Locate every Plasmodium falciparum-infected red blood cell.
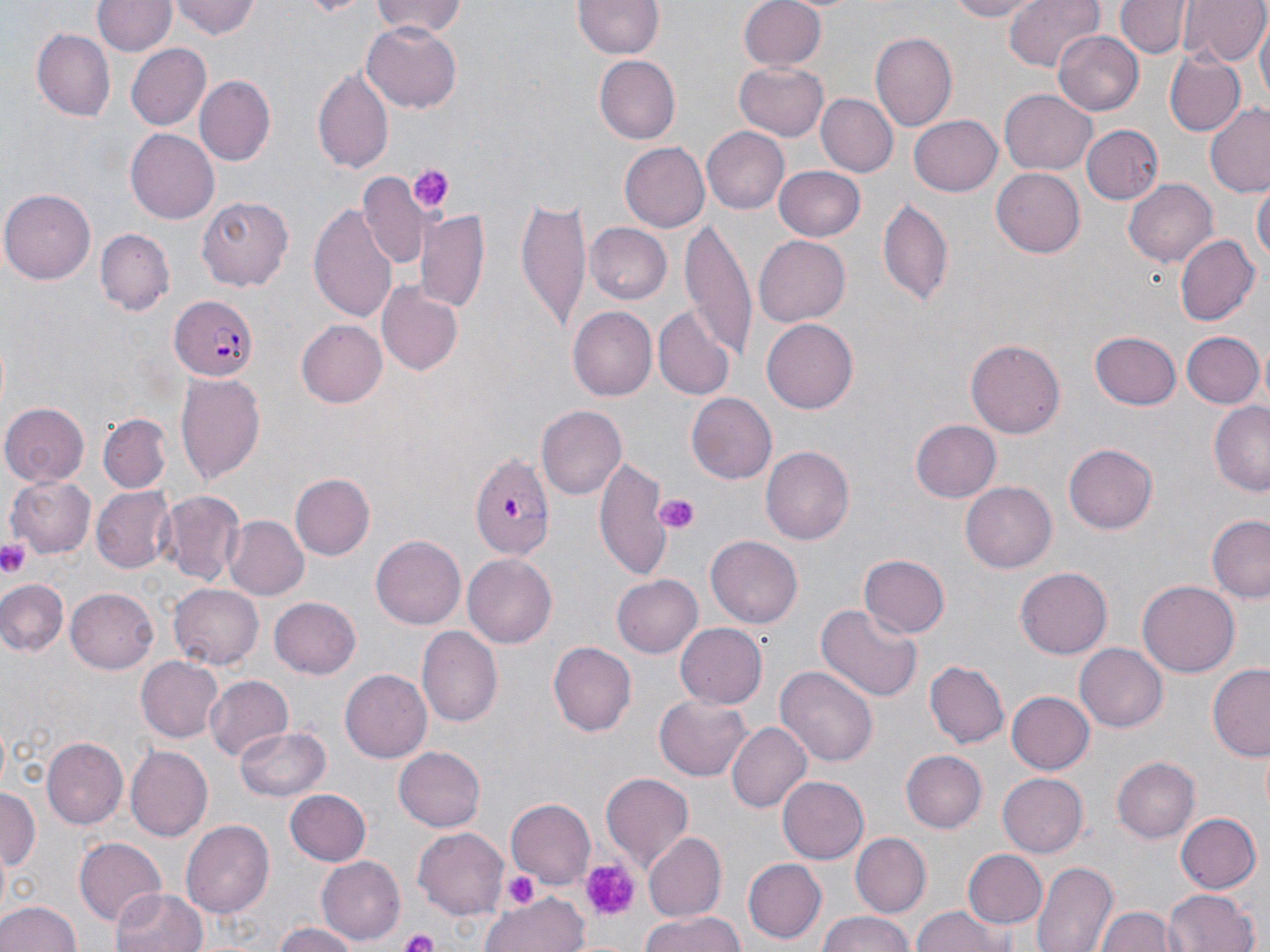
Approximate bounding boxes as (x1,y1)-(x2,y2) corner pairs in pixels.
Plasmodium falciparum-infected red blood cells: (169,294)-(260,381), (471,453)-(558,561).

slide-level diagnosis = Plasmodium falciparum
platelet locations = approximate bounding boxes as (x1,y1)-(x2,y2) corner pairs in pixels: (410,163)-(453,212), (653,492)-(701,535), (0,540)-(32,577), (577,857)-(641,920), (504,871)-(539,910), (400,929)-(441,952)
image size = 1270×952 pixels
field of view = single
magnification = 1000x
modality = optical microscopy
stain = May-Grünwald-Giemsa
uninfected red blood cell locations = approximate bounding boxes as (x1,y1)-(x2,y2) corner pairs in pixels: (170,0)-(258,41), (368,0)-(469,39), (740,0)-(826,72), (940,0)-(1047,22), (1006,0)-(1107,73), (1118,0)-(1187,59), (1179,0)-(1266,66), (92,1)-(175,57), (575,1)-(663,61), (1256,19)-(1268,109), (361,24)-(462,113), (33,27)-(115,121), (1055,30)-(1143,114), (868,33)-(956,132), (124,43)-(210,132), (1163,51)-(1245,139), (596,56)-(680,145), (735,63)-(829,141), (313,65)-(393,173), (195,75)-(273,167), (1000,88)-(1098,176), (816,93)-(896,177), (1203,104)-(1270,195), (909,113)-(1002,197), (1082,124)-(1162,203), (702,127)-(790,214), (125,129)-(218,223), (620,142)-(709,233), (774,164)-(865,240), (992,168)-(1085,257), (359,170)-(427,268), (1124,177)-(1218,268), (1252,179)-(1269,268), (2,187)-(97,283), (516,194)-(590,333), (196,195)-(294,292), (877,198)-(953,309), (310,200)-(400,323), (416,210)-(491,316), (584,223)-(672,305), (680,223)-(755,363), (95,229)-(173,315), (1174,234)-(1258,328), (753,235)-(849,326), (377,283)-(463,376), (568,306)-(657,400), (653,306)-(734,400), (295,319)-(387,408), (762,320)-(858,412), (1091,329)-(1181,410), (1182,331)-(1263,408), (967,338)-(1067,438), (174,373)-(266,484), (688,392)-(780,484), (4,401)-(90,485), (1209,403)-(1270,495), (536,406)-(626,500), (97,415)-(171,495), (911,420)-(1000,503), (1063,443)-(1158,533), (761,446)-(855,546), (593,455)-(673,583), (290,474)-(375,560), (8,475)-(96,559), (963,481)-(1056,573), (91,486)-(176,575), (157,490)-(244,584), (222,515)-(308,600), (1206,517)-(1270,602), (371,535)-(466,630), (707,536)-(802,628), (860,554)-(950,639), (464,555)-(556,647), (1016,566)-(1114,658), (611,574)-(703,659), (0,577)-(68,657), (1138,579)-(1239,679), (169,583)-(264,669), (68,588)-(160,674), (270,598)-(361,679), (815,603)-(921,705), (676,622)-(768,710), (418,626)-(502,727), (550,640)-(635,736), (1075,643)-(1165,732), (137,656)-(223,744), (925,661)-(1006,748), (775,664)-(878,767), (1207,664)-(1270,760), (341,670)-(432,762), (204,675)-(292,761), (730,688)-(849,804), (1007,691)-(1094,773), (655,694)-(754,782), (727,722)-(812,814), (236,725)-(329,802), (42,737)-(128,832), (123,746)-(211,841), (394,746)-(486,832), (901,748)-(987,831), (1113,756)-(1199,844), (601,772)-(694,871), (998,772)-(1088,858), (777,775)-(869,865), (0,789)-(40,873), (284,789)-(371,866), (505,798)-(595,886), (1176,812)-(1260,894), (181,819)-(274,920), (413,828)-(508,915), (644,831)-(726,921), (853,833)-(930,914), (74,838)-(168,926), (963,849)-(1048,930), (316,856)-(404,944), (742,858)-(827,943), (1032,859)-(1116,952), (112,888)-(208,952), (1165,889)-(1260,952), (482,893)-(591,952), (0,898)-(84,952), (910,906)-(1014,952), (1099,907)-(1175,952), (814,911)-(920,952), (635,912)-(749,952), (270,923)-(358,952)
preparation = thin blood film